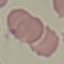
malaria status = uninfected
capture = smartphone camera at the microscope eyepiece
preparation = thin smear
stain = Giemsa
image type = automatically extracted cell patch, resized to 64 × 64 pixels